Name the parasite shown.
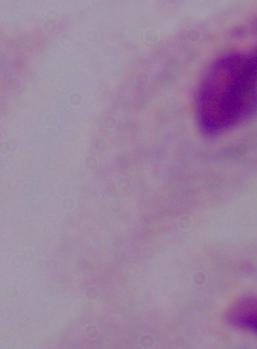

This is a trichomonad.

1000x magnification. Photomicrograph.